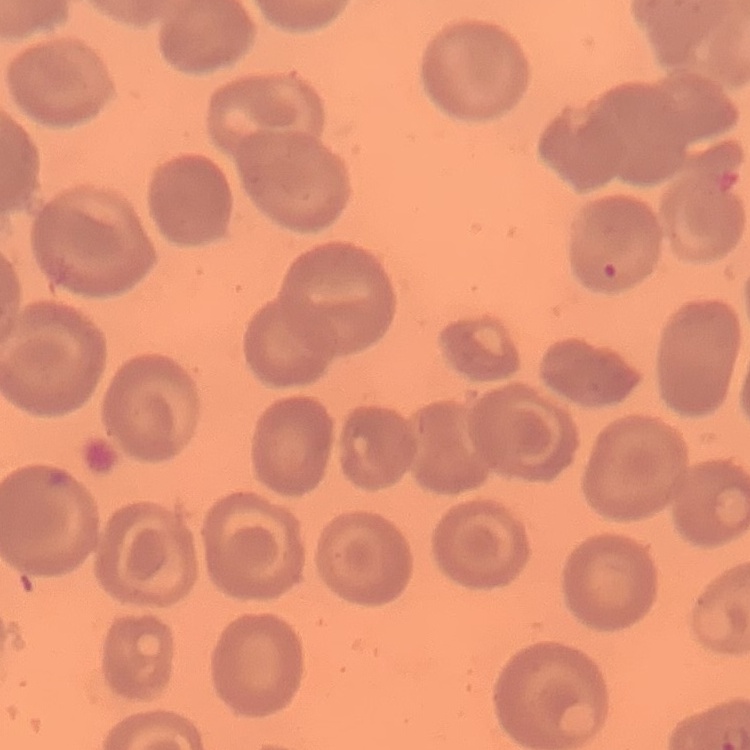

The red blood cells exhibit no rouleaux formation. Thin peripheral smear. Stained with either Field's or Giemsa. One tile cut from a larger photomicrograph.